Give the extent of all Plasmodium falciparum-infected red blood cells.
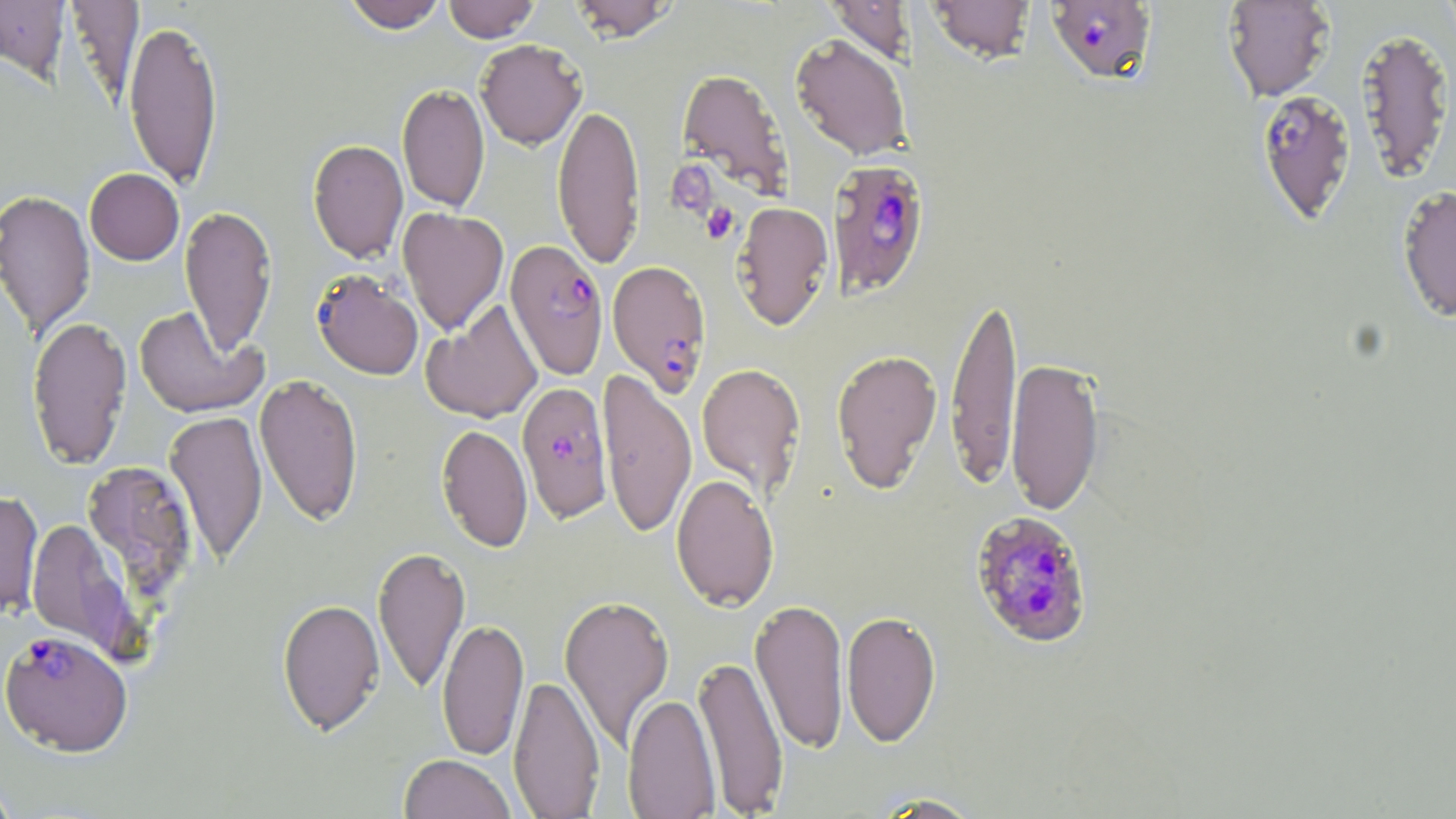

Approximate bounding boxes as [x1, y1, x2, y2] in pixels.
Plasmodium falciparum-infected red blood cells: [1046, 1, 1157, 85], [1256, 89, 1357, 226], [827, 158, 930, 298], [505, 239, 609, 379], [607, 259, 712, 395], [311, 269, 424, 380], [517, 381, 613, 522], [969, 510, 1094, 649], [1, 629, 133, 756].

{
  "slide_level_diagnosis": "Plasmodium falciparum",
  "platelet_locations": "approximate bounding boxes as [x1, y1, x2, y2] in pixels: [701, 202, 739, 244]",
  "stain": "May-Grünwald-Giemsa",
  "modality": "light microscopy",
  "uninfected_red_blood_cell_locations": "approximate bounding boxes as [x1, y1, x2, y2] in pixels: [64, 0, 144, 105], [341, 0, 449, 33], [443, 0, 541, 42], [568, 0, 679, 42], [926, 0, 1037, 64], [1222, 0, 1336, 102], [0, 1, 70, 80], [824, 1, 915, 66], [123, 17, 224, 190], [1356, 25, 1455, 184], [790, 33, 911, 162], [475, 39, 587, 150], [676, 68, 794, 201], [397, 82, 490, 214], [552, 101, 645, 271], [307, 139, 408, 263], [85, 168, 184, 265], [1396, 185, 1456, 323], [0, 188, 95, 341], [732, 201, 833, 331], [180, 204, 277, 357], [397, 207, 508, 336], [945, 291, 1023, 492], [421, 300, 542, 424], [134, 306, 267, 418], [26, 315, 132, 470], [830, 348, 943, 494], [1005, 356, 1104, 517], [696, 362, 806, 499], [598, 367, 698, 539], [254, 373, 364, 527], [165, 409, 268, 566], [436, 423, 532, 552], [82, 459, 199, 604], [671, 474, 779, 612], [0, 490, 44, 618], [25, 519, 141, 660], [373, 546, 471, 695], [559, 593, 674, 753], [750, 597, 849, 754], [277, 598, 385, 736], [842, 610, 941, 747], [437, 617, 529, 760], [693, 653, 789, 815], [509, 673, 605, 818], [622, 693, 721, 818], [399, 754, 517, 819], [0, 773, 20, 818], [868, 792, 986, 818]",
  "field_of_view": "single",
  "preparation": "thin blood film",
  "image_size": "1456×819 pixels",
  "magnification": "1000x"
}